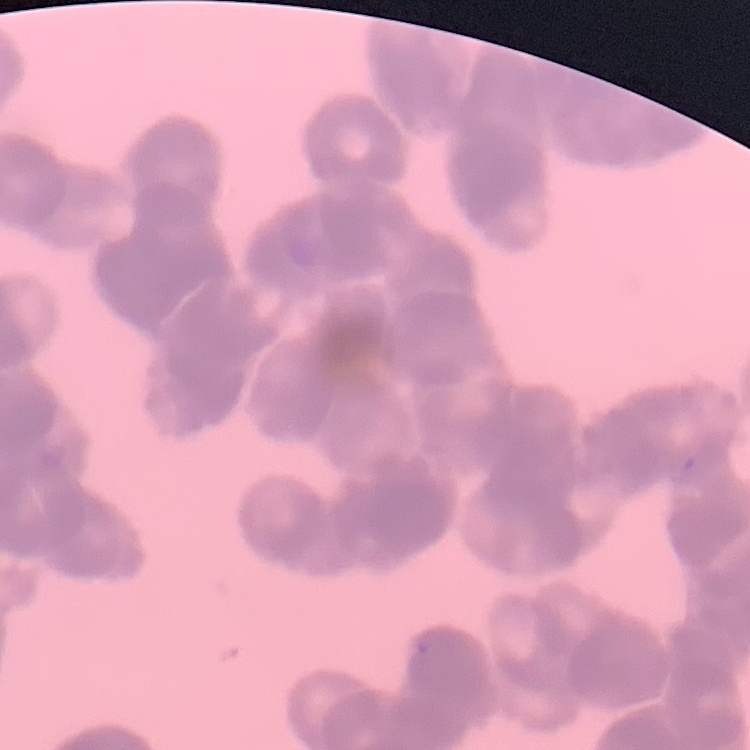
red blood cell morphology = rouleaux formation
image type = one tile cut from a larger photomicrograph
preparation = thin blood smear
stain = Field's or Giemsa